Give the extent of all Plasmodium falciparum-infected red blood cells.
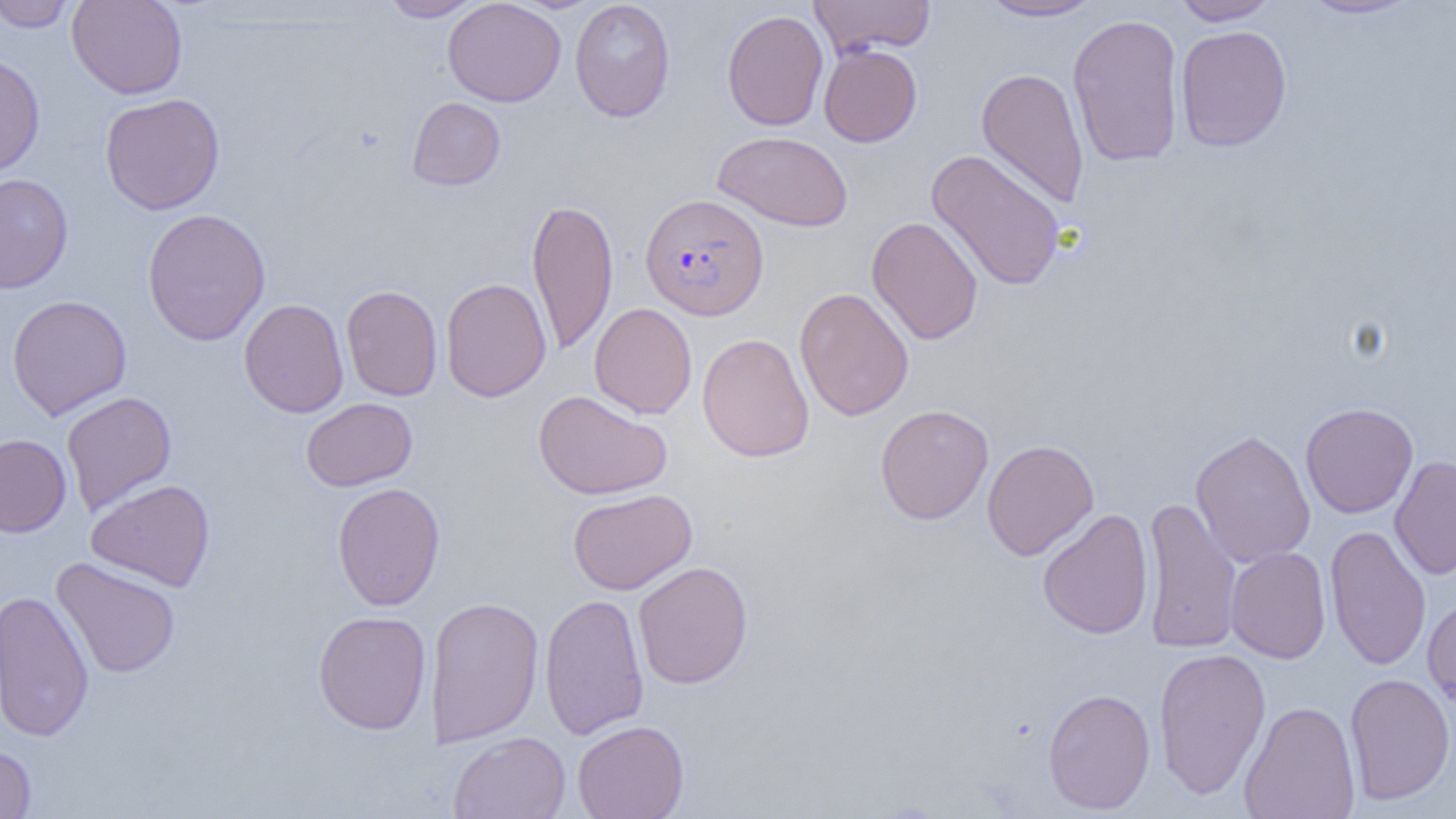
Approximate bounding boxes as [x1, y1, x2, y2] in pixels.
Plasmodium falciparum-infected red blood cells: [640, 193, 769, 321].

Summary:
  - Uninfected red blood cell locations: [0, 0, 77, 32], [66, 0, 187, 99], [378, 0, 483, 21], [442, 0, 567, 107], [569, 0, 676, 123], [808, 0, 934, 59], [976, 0, 1108, 22], [1169, 0, 1282, 25], [1297, 0, 1423, 21], [721, 9, 829, 131], [1067, 13, 1185, 168], [1175, 24, 1292, 152], [819, 44, 922, 147], [0, 53, 45, 178], [976, 66, 1090, 211], [100, 93, 225, 215], [407, 97, 505, 190], [712, 130, 853, 232], [926, 149, 1067, 291], [0, 173, 73, 293], [527, 197, 619, 355], [142, 208, 271, 346], [866, 216, 984, 345], [440, 277, 551, 402], [341, 284, 443, 401], [794, 287, 914, 421], [6, 294, 132, 420], [239, 298, 349, 418], [589, 303, 697, 419], [697, 333, 814, 462], [533, 389, 672, 500], [61, 391, 177, 516], [301, 398, 417, 491], [1301, 402, 1419, 518], [875, 404, 994, 525], [1190, 429, 1315, 568], [0, 434, 71, 537], [982, 439, 1099, 561], [1390, 455, 1456, 580], [86, 478, 216, 592], [332, 482, 446, 611], [567, 488, 697, 595], [1140, 496, 1242, 655], [1037, 508, 1153, 640], [1324, 524, 1431, 671], [1225, 546, 1331, 664], [51, 557, 181, 678], [633, 561, 754, 689], [0, 589, 95, 742], [539, 593, 649, 740], [1422, 594, 1456, 712], [425, 595, 544, 747], [313, 610, 432, 735], [1153, 647, 1271, 801], [1344, 673, 1455, 806], [1042, 687, 1156, 814], [1238, 700, 1362, 819], [573, 720, 689, 819], [448, 731, 571, 818], [0, 743, 36, 818]
  - Slide-level diagnosis: Plasmodium falciparum
  - Field of view: single
  - Preparation: thin blood smear
  - Image size: 1456×819 pixels
  - Magnification: 1000x
  - Modality: light microscopy